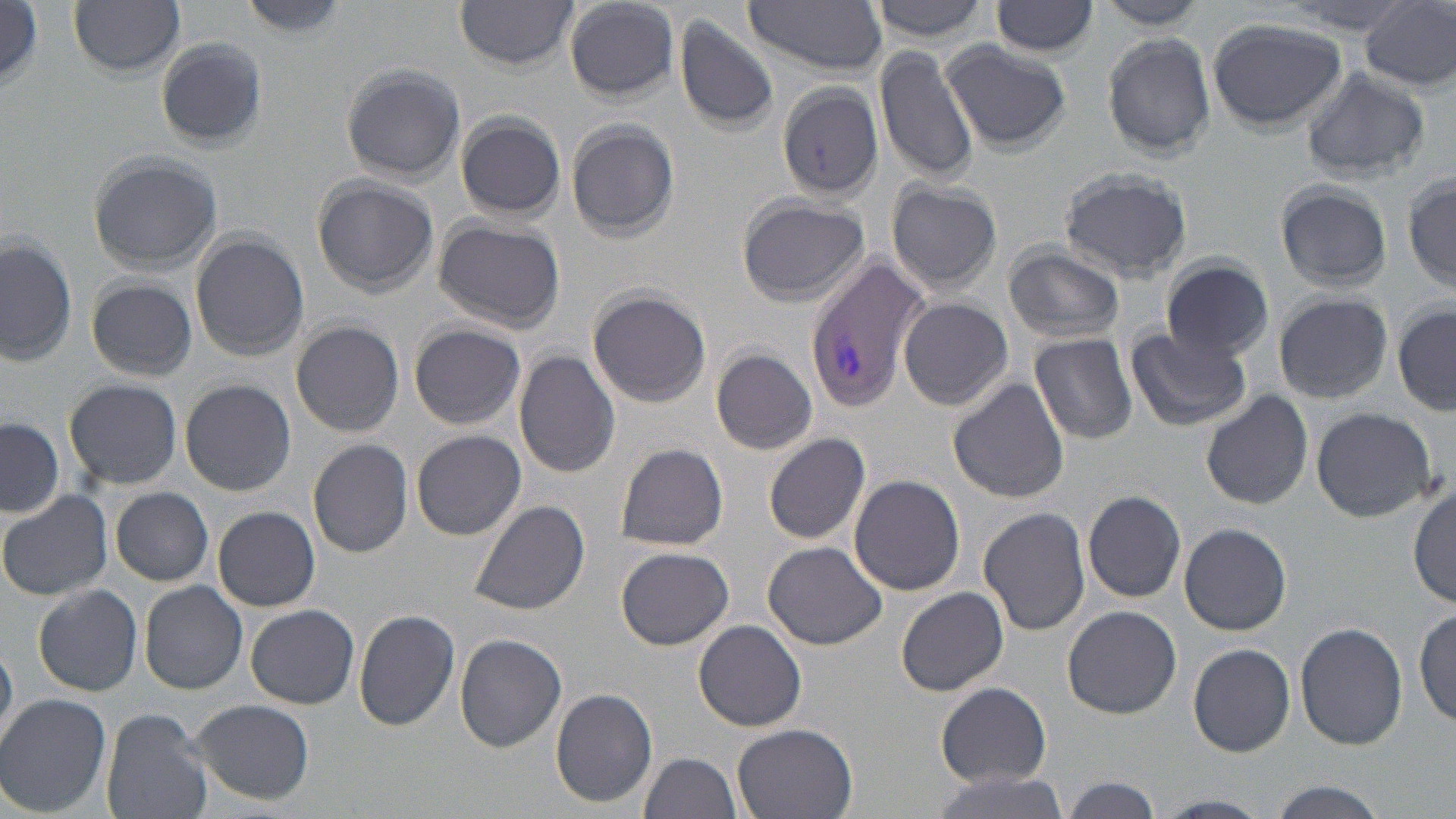

Summary:
  - Coordinate format: approximate bounding boxes as (x1, y1, x2, y2) in pixels
  - Uninfected red blood cell locations: (71, 0, 186, 76), (240, 0, 348, 36), (454, 0, 579, 67), (868, 0, 993, 44), (563, 1, 682, 101), (742, 2, 889, 75), (990, 2, 1101, 58), (1359, 2, 1456, 94), (2, 3, 44, 87), (1093, 3, 1210, 31), (673, 13, 781, 135), (1205, 17, 1349, 133), (1101, 31, 1216, 160), (156, 37, 268, 152), (942, 39, 1070, 153), (873, 44, 979, 183), (340, 64, 467, 186), (1299, 68, 1431, 183), (776, 82, 885, 202), (454, 112, 567, 221), (566, 118, 680, 242), (90, 153, 223, 274), (1058, 166, 1194, 282), (1403, 172, 1456, 295), (311, 174, 438, 299), (885, 180, 1003, 297), (1274, 182, 1392, 294), (735, 193, 870, 307), (433, 218, 565, 333), (189, 231, 309, 361), (0, 234, 76, 371), (1002, 244, 1126, 348), (1160, 257, 1275, 361), (86, 276, 197, 382), (586, 286, 712, 409), (1271, 290, 1394, 406), (898, 298, 1015, 413), (1391, 301, 1455, 417), (290, 321, 404, 437), (409, 323, 526, 431), (1126, 328, 1250, 432), (1030, 332, 1137, 444), (981, 344, 1097, 471), (711, 347, 818, 455), (513, 349, 621, 479), (64, 377, 182, 491), (947, 377, 1069, 504), (179, 378, 296, 497), (1201, 390, 1313, 509), (1310, 406, 1437, 524), (0, 416, 65, 521), (411, 429, 525, 541), (762, 433, 872, 545), (308, 438, 414, 558), (613, 442, 729, 553), (848, 474, 966, 595), (1411, 480, 1456, 609), (111, 486, 213, 586), (0, 488, 113, 601), (1082, 489, 1187, 603), (470, 498, 590, 615), (212, 506, 321, 612), (978, 506, 1091, 636), (1179, 522, 1291, 637), (764, 541, 886, 650), (616, 545, 734, 651), (138, 580, 249, 694), (32, 582, 143, 696), (895, 586, 1009, 697), (245, 604, 360, 709), (1062, 605, 1181, 718), (352, 607, 461, 732), (1414, 607, 1455, 726), (692, 618, 808, 731), (1296, 621, 1408, 752), (455, 632, 567, 752), (0, 641, 17, 747), (1187, 643, 1296, 757), (935, 682, 1051, 787), (550, 688, 659, 809), (0, 694, 113, 816), (191, 698, 315, 806), (99, 708, 212, 819), (731, 723, 859, 819), (637, 752, 744, 819), (925, 768, 1076, 818), (1057, 777, 1166, 817), (1259, 782, 1397, 819)
  - Plasmodium vivax-infected red blood cell locations: (804, 256, 926, 411)
  - Slide-level diagnosis: Plasmodium vivax
  - Image size: 1456×819 pixels
  - Preparation: thin blood film
  - Magnification: 1000x
  - Modality: optical microscopy
  - Stain: May-Grünwald-Giemsa
  - Field of view: one of a larger specimen